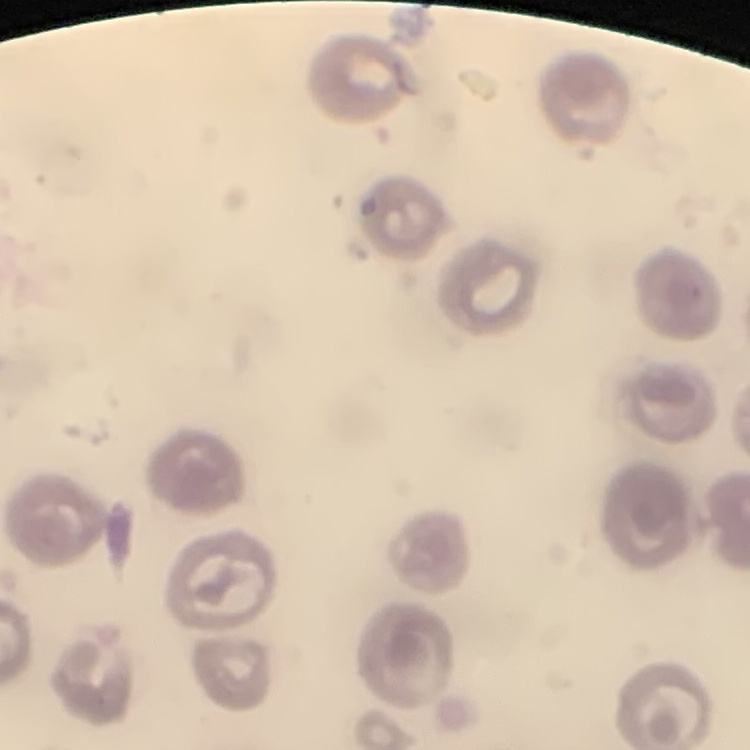

The red blood cells show no rouleaux formation. One tile cut from a larger photomicrograph. Field's or Giemsa stain. Thin blood film.